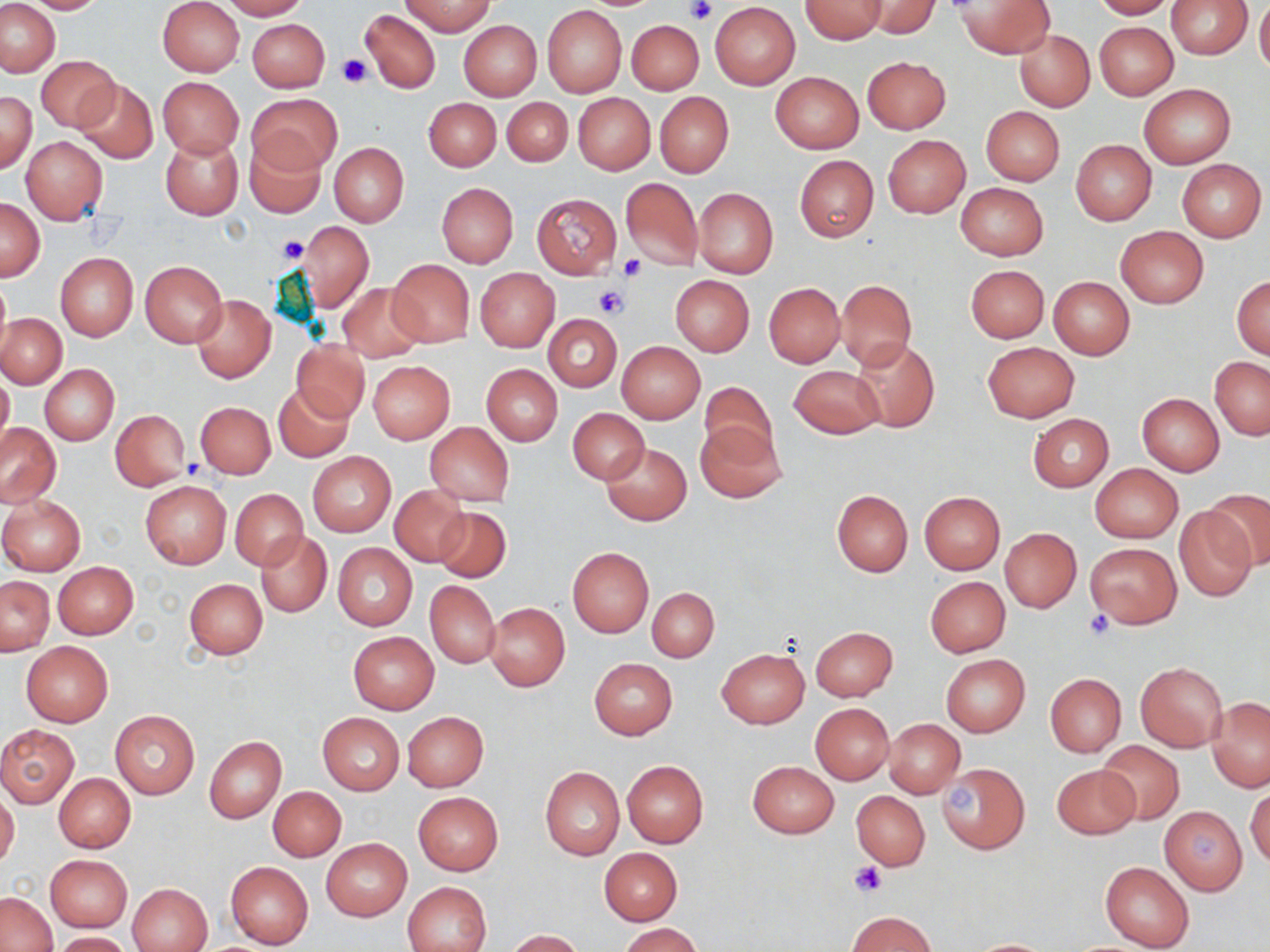

{
  "slide_level_diagnosis": "negative for blood parasites",
  "magnification": "1000x",
  "modality": "optical microscopy",
  "platelet_locations": "approximate bounding boxes as named x1/y1/x2/y2 corners in pixels: (x1=682, y1=0, x2=715, y2=23), (x1=336, y1=54, x2=370, y2=89), (x1=278, y1=234, x2=307, y2=264), (x1=618, y1=253, x2=646, y2=280), (x1=594, y1=286, x2=626, y2=318), (x1=182, y1=455, x2=208, y2=480), (x1=1084, y1=609, x2=1115, y2=639), (x1=851, y1=862, x2=887, y2=898)",
  "preparation": "thin blood smear",
  "stain": "May-Grünwald-Giemsa",
  "field_of_view": "one of a larger specimen",
  "image_size": "1270×952 pixels",
  "uninfected_red_blood_cell_locations": "approximate bounding boxes as named x1/y1/x2/y2 corners in pixels: (x1=21, y1=0, x2=107, y2=14), (x1=158, y1=0, x2=245, y2=77), (x1=219, y1=0, x2=307, y2=19), (x1=863, y1=0, x2=939, y2=37), (x1=957, y1=0, x2=1054, y2=57), (x1=1092, y1=0, x2=1177, y2=19), (x1=1165, y1=0, x2=1253, y2=58), (x1=1, y1=1, x2=60, y2=77), (x1=401, y1=1, x2=496, y2=36), (x1=800, y1=1, x2=886, y2=43), (x1=1255, y1=1, x2=1270, y2=77), (x1=710, y1=2, x2=801, y2=90), (x1=543, y1=5, x2=626, y2=96), (x1=360, y1=8, x2=441, y2=94), (x1=247, y1=18, x2=329, y2=91), (x1=625, y1=18, x2=707, y2=97), (x1=458, y1=19, x2=542, y2=100), (x1=1094, y1=21, x2=1178, y2=100), (x1=1014, y1=29, x2=1095, y2=112), (x1=37, y1=55, x2=120, y2=132), (x1=863, y1=56, x2=950, y2=133), (x1=770, y1=72, x2=864, y2=154), (x1=158, y1=77, x2=243, y2=158), (x1=74, y1=79, x2=158, y2=164), (x1=1139, y1=84, x2=1235, y2=167), (x1=0, y1=91, x2=37, y2=174), (x1=249, y1=91, x2=339, y2=174), (x1=655, y1=92, x2=734, y2=178), (x1=572, y1=93, x2=655, y2=174), (x1=424, y1=97, x2=501, y2=171), (x1=502, y1=97, x2=572, y2=167), (x1=981, y1=106, x2=1064, y2=185), (x1=161, y1=135, x2=243, y2=220), (x1=883, y1=135, x2=970, y2=218), (x1=22, y1=136, x2=107, y2=223), (x1=245, y1=137, x2=326, y2=218), (x1=1071, y1=139, x2=1156, y2=225), (x1=328, y1=142, x2=409, y2=227), (x1=794, y1=154, x2=879, y2=241), (x1=1176, y1=159, x2=1267, y2=242), (x1=621, y1=178, x2=702, y2=271), (x1=437, y1=182, x2=518, y2=269), (x1=956, y1=182, x2=1048, y2=260), (x1=693, y1=187, x2=778, y2=279), (x1=531, y1=193, x2=621, y2=278), (x1=1, y1=198, x2=45, y2=281), (x1=301, y1=222, x2=373, y2=311), (x1=1116, y1=226, x2=1208, y2=308), (x1=55, y1=253, x2=138, y2=340), (x1=387, y1=258, x2=474, y2=347), (x1=140, y1=260, x2=228, y2=347), (x1=965, y1=264, x2=1049, y2=343), (x1=474, y1=268, x2=559, y2=351), (x1=670, y1=275, x2=754, y2=355), (x1=1232, y1=276, x2=1269, y2=360), (x1=0, y1=277, x2=11, y2=357), (x1=1048, y1=277, x2=1135, y2=358), (x1=837, y1=278, x2=916, y2=369), (x1=337, y1=282, x2=426, y2=361), (x1=763, y1=282, x2=846, y2=367), (x1=192, y1=294, x2=276, y2=383), (x1=1, y1=314, x2=66, y2=388), (x1=544, y1=314, x2=622, y2=391), (x1=851, y1=337, x2=939, y2=432), (x1=291, y1=339, x2=369, y2=422), (x1=616, y1=341, x2=705, y2=424), (x1=982, y1=341, x2=1079, y2=421), (x1=1210, y1=357, x2=1269, y2=439), (x1=368, y1=361, x2=454, y2=443), (x1=39, y1=364, x2=119, y2=445), (x1=481, y1=364, x2=562, y2=445), (x1=790, y1=364, x2=884, y2=438), (x1=0, y1=371, x2=13, y2=454), (x1=700, y1=381, x2=779, y2=464), (x1=274, y1=383, x2=354, y2=462), (x1=1136, y1=393, x2=1225, y2=476), (x1=195, y1=401, x2=275, y2=478), (x1=109, y1=409, x2=191, y2=490), (x1=568, y1=409, x2=649, y2=484), (x1=1028, y1=413, x2=1114, y2=492), (x1=0, y1=422, x2=61, y2=507), (x1=424, y1=422, x2=514, y2=507), (x1=697, y1=423, x2=784, y2=503), (x1=602, y1=442, x2=692, y2=525), (x1=308, y1=452, x2=395, y2=536), (x1=1090, y1=463, x2=1184, y2=543), (x1=140, y1=480, x2=231, y2=568), (x1=389, y1=485, x2=471, y2=566), (x1=1207, y1=488, x2=1270, y2=571), (x1=231, y1=489, x2=308, y2=569), (x1=831, y1=489, x2=914, y2=577), (x1=919, y1=492, x2=1004, y2=573), (x1=0, y1=497, x2=85, y2=575), (x1=434, y1=505, x2=510, y2=582), (x1=1174, y1=508, x2=1257, y2=602), (x1=1000, y1=529, x2=1081, y2=612), (x1=257, y1=531, x2=331, y2=616), (x1=1084, y1=542, x2=1181, y2=629), (x1=333, y1=544, x2=418, y2=631), (x1=567, y1=547, x2=653, y2=637), (x1=53, y1=561, x2=138, y2=639), (x1=0, y1=575, x2=54, y2=655), (x1=925, y1=576, x2=1011, y2=657), (x1=185, y1=578, x2=267, y2=659), (x1=425, y1=580, x2=501, y2=668), (x1=647, y1=588, x2=719, y2=662), (x1=485, y1=603, x2=570, y2=691), (x1=810, y1=626, x2=898, y2=701), (x1=347, y1=631, x2=439, y2=713), (x1=21, y1=641, x2=112, y2=726), (x1=717, y1=648, x2=809, y2=728), (x1=942, y1=654, x2=1029, y2=737), (x1=590, y1=659, x2=677, y2=739), (x1=1135, y1=661, x2=1228, y2=752), (x1=1045, y1=673, x2=1126, y2=757), (x1=1207, y1=696, x2=1270, y2=792), (x1=811, y1=703, x2=894, y2=784), (x1=109, y1=710, x2=200, y2=798), (x1=402, y1=711, x2=488, y2=791), (x1=318, y1=712, x2=403, y2=794), (x1=885, y1=719, x2=964, y2=798), (x1=0, y1=724, x2=78, y2=807), (x1=204, y1=736, x2=285, y2=824), (x1=1095, y1=739, x2=1185, y2=827), (x1=748, y1=760, x2=839, y2=838), (x1=622, y1=761, x2=708, y2=849), (x1=937, y1=762, x2=1030, y2=853), (x1=1051, y1=763, x2=1141, y2=840), (x1=540, y1=766, x2=624, y2=859), (x1=54, y1=774, x2=135, y2=852), (x1=268, y1=787, x2=346, y2=860), (x1=1247, y1=787, x2=1270, y2=869), (x1=0, y1=790, x2=19, y2=869), (x1=852, y1=790, x2=930, y2=871), (x1=413, y1=793, x2=503, y2=876), (x1=1158, y1=807, x2=1246, y2=895), (x1=322, y1=838, x2=412, y2=921), (x1=600, y1=847, x2=681, y2=925), (x1=46, y1=855, x2=132, y2=932), (x1=226, y1=861, x2=314, y2=948), (x1=1100, y1=861, x2=1194, y2=952), (x1=404, y1=881, x2=490, y2=952), (x1=127, y1=883, x2=213, y2=952), (x1=1, y1=891, x2=58, y2=952), (x1=847, y1=910, x2=938, y2=951), (x1=619, y1=923, x2=703, y2=952), (x1=505, y1=929, x2=582, y2=952), (x1=54, y1=932, x2=131, y2=951), (x1=967, y1=938, x2=1055, y2=951)"
}